Name the blood parasite species.
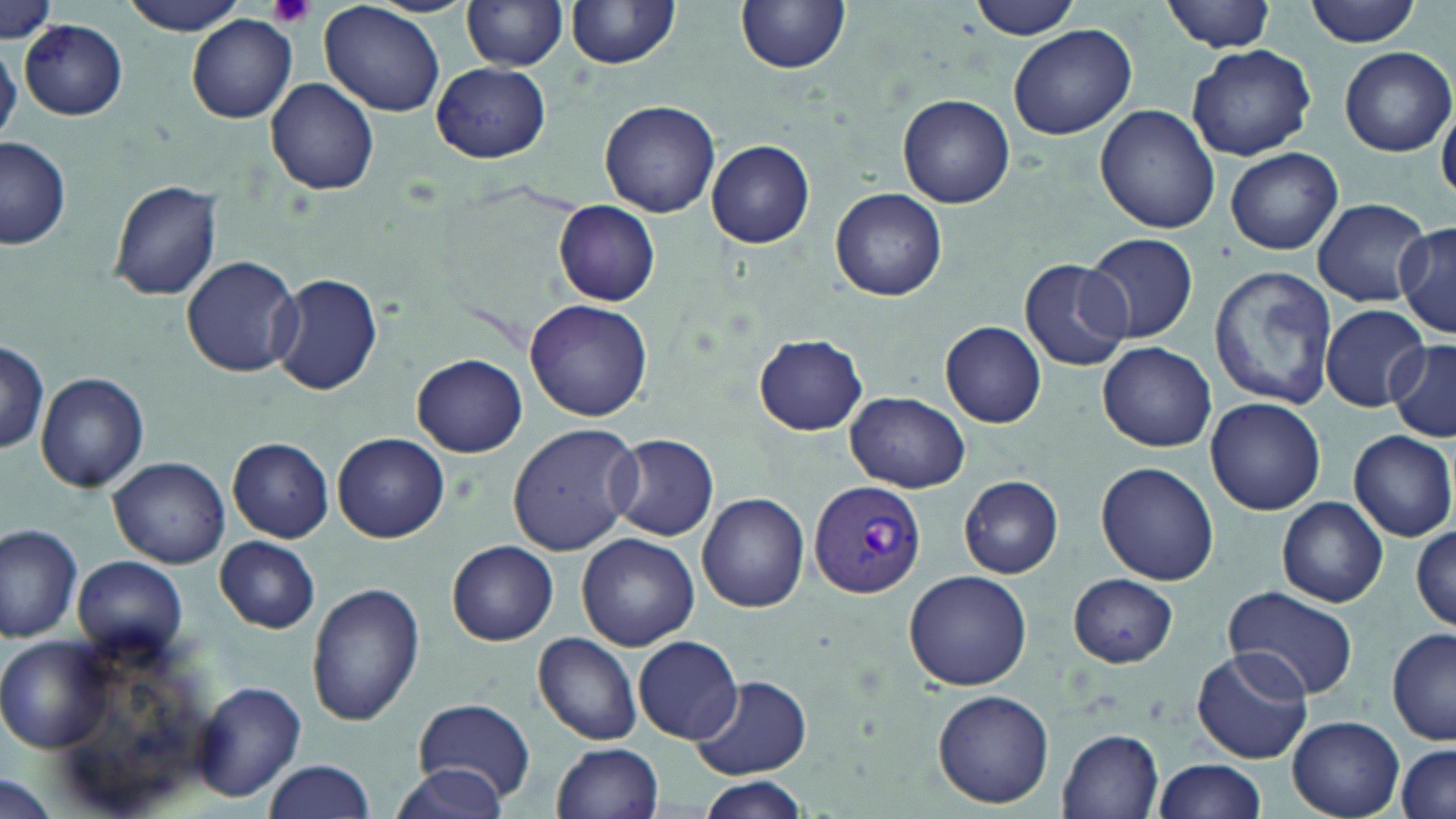

Plasmodium vivax.

magnification: 1000x
platelet_locations: 'approximate bounding boxes as (x1, y1, x2, y2) in pixels: (266, 0, 316, 29)'
field_of_view: one of a larger specimen
uninfected_red_blood_cell_locations: 'approximate bounding boxes as (x1, y1, x2, y2) in pixels: (0, 0, 61, 47), (118, 0, 251, 34), (461, 0, 571, 71), (565, 0, 683, 70), (968, 0, 1086, 41), (1163, 0, 1277, 53), (1306, 0, 1423, 46), (320, 1, 447, 116), (736, 1, 850, 74), (187, 15, 298, 123), (20, 19, 128, 120), (1009, 25, 1137, 140), (0, 41, 22, 145), (1187, 44, 1317, 161), (1339, 46, 1454, 156), (432, 63, 550, 162), (266, 78, 380, 195), (898, 94, 1015, 207), (598, 99, 720, 217), (1437, 99, 1456, 204), (1095, 103, 1221, 233), (1, 136, 72, 252), (707, 139, 815, 248), (1224, 147, 1344, 256), (108, 179, 224, 302), (830, 187, 948, 301), (1313, 198, 1430, 306), (553, 200, 662, 307), (1394, 219, 1455, 340), (1085, 233, 1198, 345), (182, 254, 302, 377), (1019, 257, 1133, 372), (1210, 267, 1337, 409), (270, 275, 382, 395), (525, 301, 654, 422), (1320, 305, 1428, 411), (941, 321, 1046, 427), (754, 333, 867, 435), (1386, 339, 1456, 443), (1098, 341, 1216, 452), (0, 342, 50, 455), (412, 354, 527, 457), (36, 371, 149, 493), (845, 391, 969, 492), (1206, 397, 1326, 515), (507, 424, 641, 555), (1350, 430, 1455, 541), (334, 432, 449, 543), (609, 433, 719, 542), (228, 437, 334, 542), (108, 456, 231, 567), (1096, 461, 1219, 585), (959, 475, 1064, 578), (697, 490, 809, 612), (1277, 498, 1388, 607), (1411, 520, 1455, 631), (0, 522, 84, 642), (577, 534, 698, 650), (214, 537, 320, 632), (447, 541, 557, 644), (72, 554, 188, 659), (905, 569, 1031, 690), (1069, 573, 1177, 667), (306, 583, 425, 729), (1223, 586, 1359, 700), (1388, 629, 1455, 747), (533, 633, 643, 746), (0, 636, 113, 749), (633, 636, 741, 743), (1191, 646, 1311, 766), (689, 674, 809, 779), (191, 680, 308, 803), (932, 691, 1054, 806), (410, 697, 537, 803), (1287, 716, 1403, 819), (1059, 729, 1164, 817), (552, 742, 665, 819), (1392, 745, 1454, 819), (1154, 758, 1266, 818), (262, 760, 375, 817), (389, 761, 508, 818), (0, 777, 61, 819), (696, 778, 807, 817)'
preparation: thin blood smear
modality: light microscopy
image_size: 1456×819 pixels
plasmodium_vivax_infected_red_blood_cell_locations: 'approximate bounding boxes as (x1, y1, x2, y2) in pixels: (808, 479, 926, 601)'
stain: May-Grünwald-Giemsa